Assess the morphology of the red blood cells.
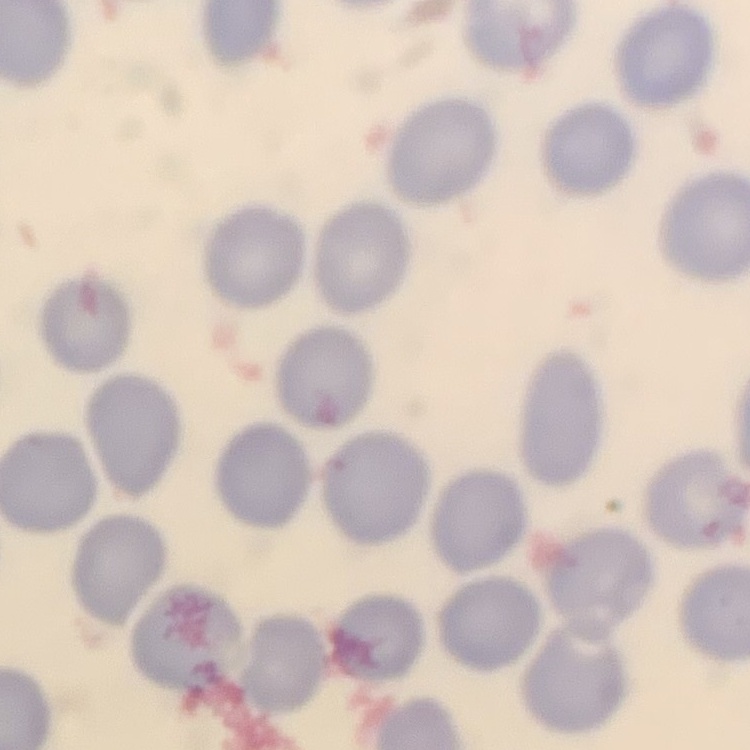
They show no rouleaux formation.

One tile cut from a larger photomicrograph. Stained with either Field's or Giemsa. Thin peripheral smear.